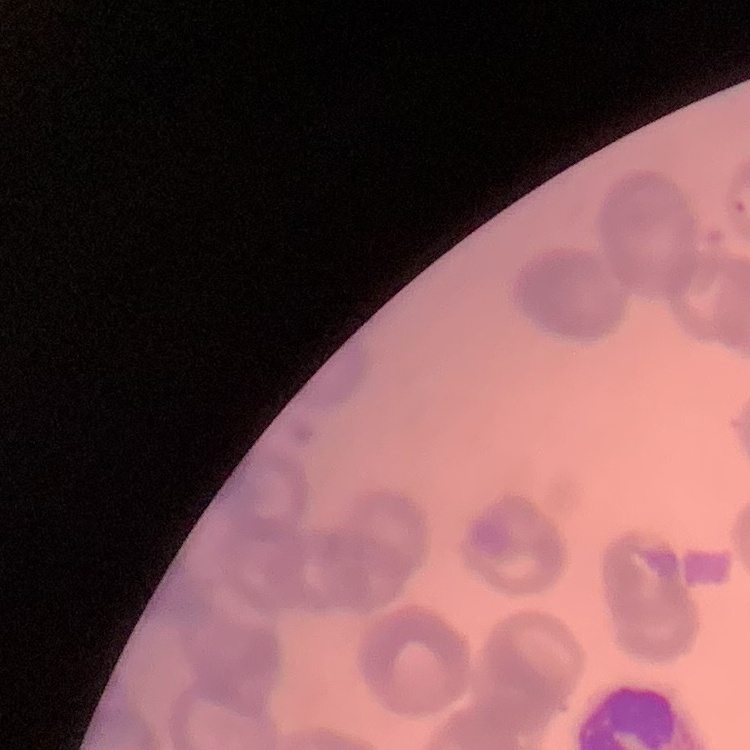
Summary:
  - Red blood cell morphology: rouleaux formation
  - Stain: Field's or Giemsa
  - Image type: square crop of a larger photomicrograph
  - Preparation: thin blood smear